Report the malaria status.
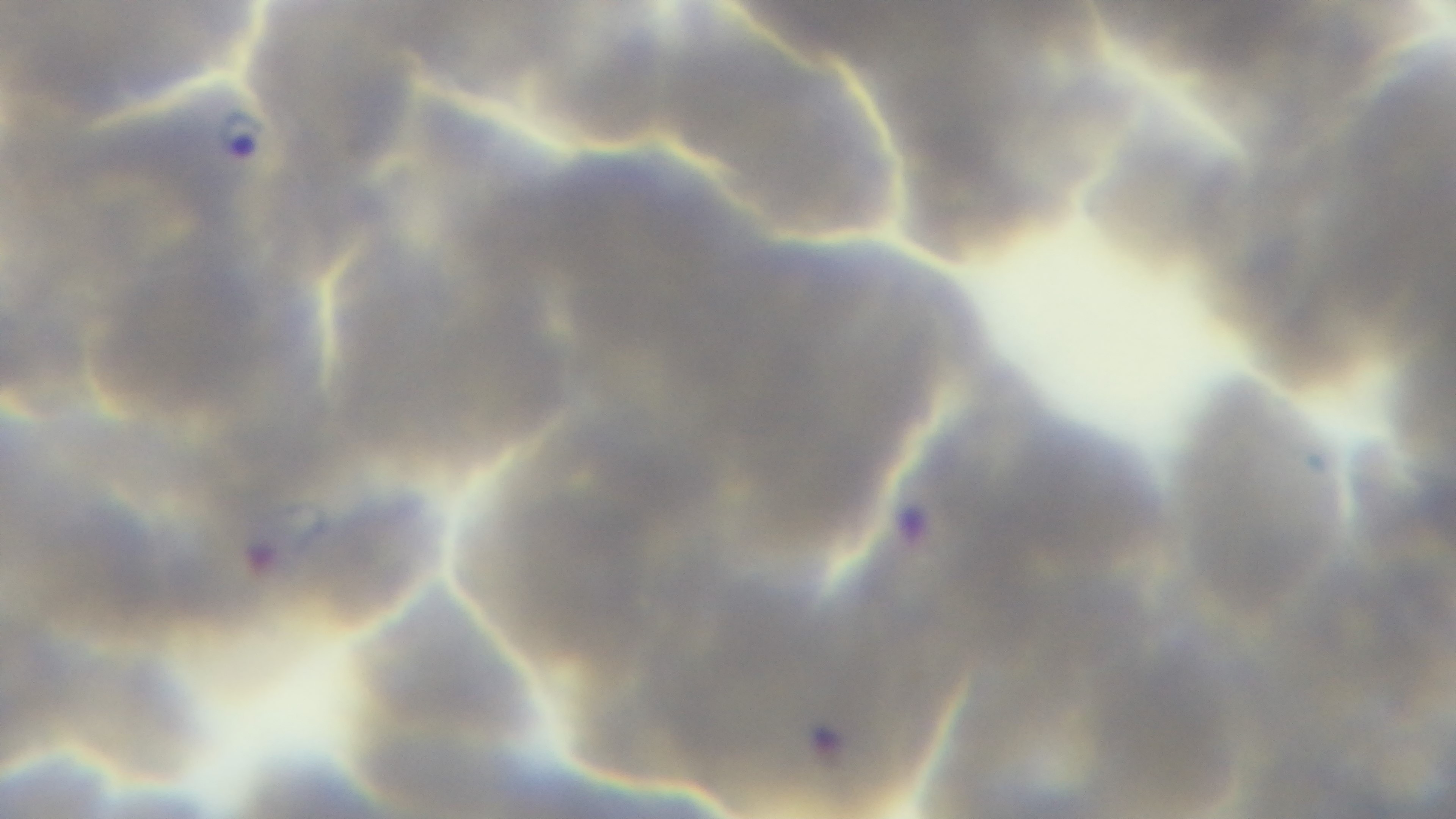
Infected.

field of view = single
objective = 100x oil immersion
preparation = thin
modality = light microscopy
capture = mounted 4K digital camera
stain = Giemsa